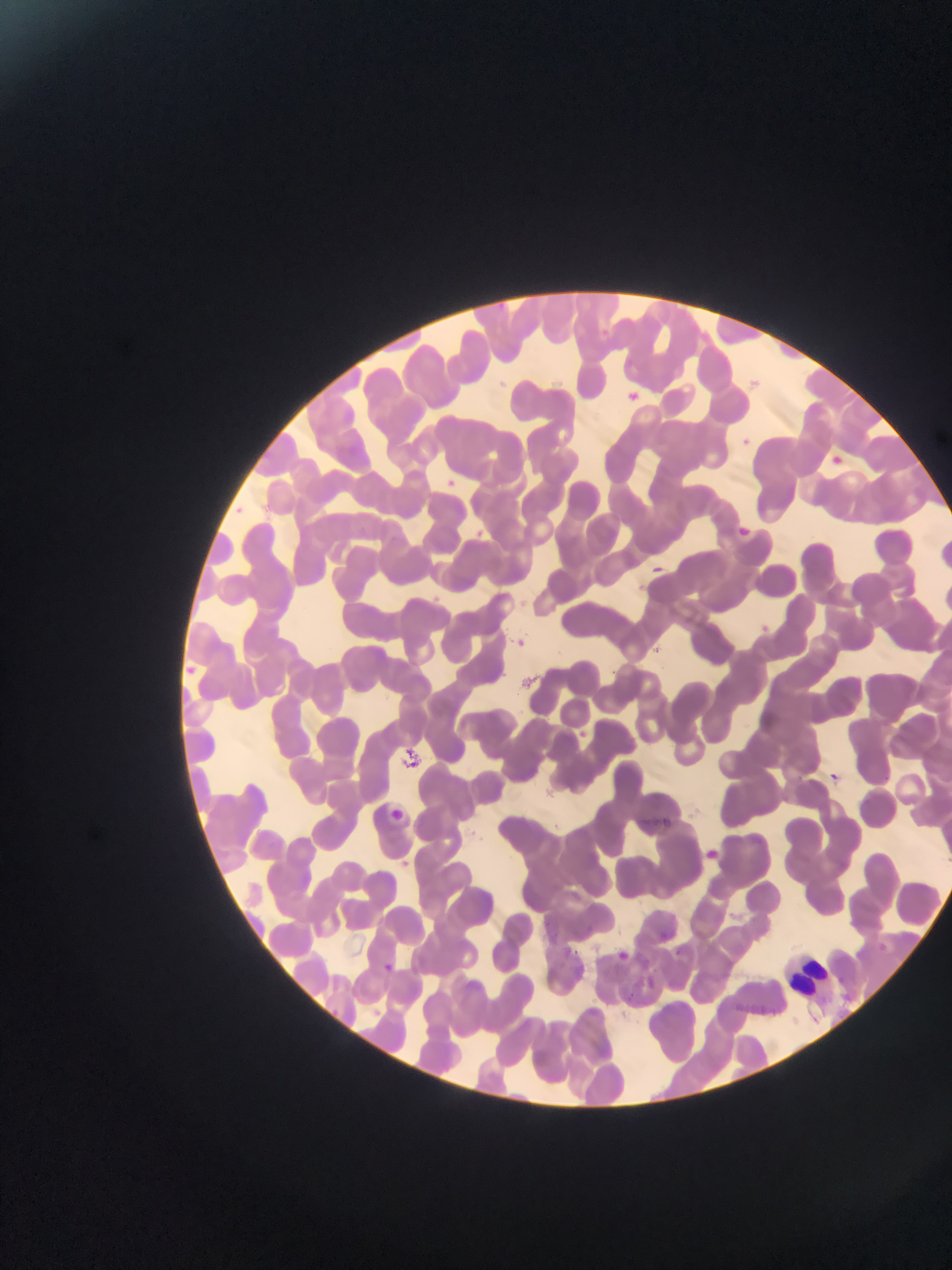

field of view = single
Plasmodium parasite locations = approximate bounding boxes as {left, top, right, bottom} in pixels (subset; some below the resolvable size): {737, 522, 754, 537}, {652, 562, 669, 571}, {756, 621, 773, 636}, {509, 635, 529, 653}, {829, 766, 841, 783}, {388, 800, 405, 827}, {696, 843, 726, 867}, {615, 944, 630, 959}, {676, 946, 685, 958}, {379, 959, 397, 976}, {328, 1005, 344, 1020}, {367, 1005, 384, 1021}
image size = 952×1270 pixels
country = Ghana
capture = mobile-phone photograph through a microscope
leukocyte locations = approximate bounding boxes as {left, top, right, bottom} in pixels: {772, 940, 832, 994}
preparation = thin blood smear